Assess this cell for malaria.
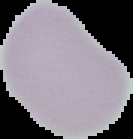
It is uninfected.

{
  "image_size": "133×139 pixels",
  "image_type": "segmented cell region on a black background",
  "preparation": "thin blood film"
}